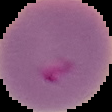

Summary:
  - Image size: 112×112 pixels
  - Result: Plasmodium parasites identified
  - Preparation: thin blood film
  - Image type: segmented cell region with the area outside set to black